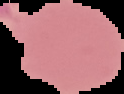
Image is 124×94 pixels. Cell region segmented out of the field of view; the surrounding area is masked to black. Malaria status: uninfected. From a thin blood film.